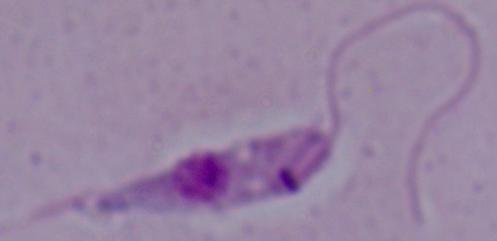
modality = micrograph
identification = Leishmania
magnification = 1000x